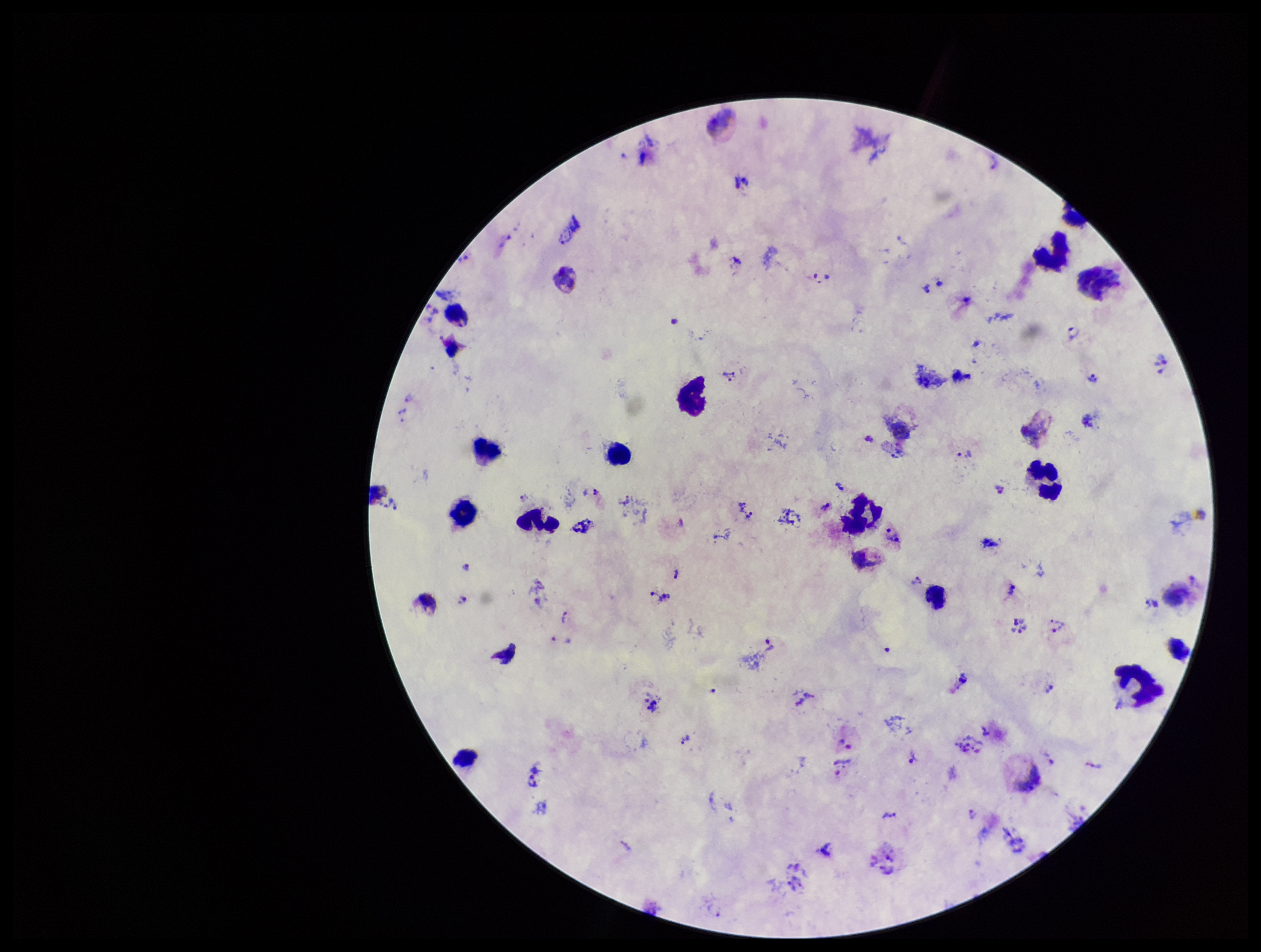
Summary:
  - Leukocyte count: 15
  - Stain: Giemsa
  - Patient malaria status: infected
  - Preparation: thick blood smear
  - Field of view: single
  - Parasite count: 33
  - Species reported for this patient: Plasmodium vivax
  - Image size: 1261×952 pixels
  - Plasmodium parasites: identified
  - Capture: smartphone photograph through the microscope eyepiece